Report the malaria status of this cell.
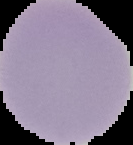
It is uninfected.

preparation = thin blood film
image size = 133×145 pixels
image type = segmented cell region on a black background